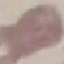
Summary:
  - Malaria status: uninfected
  - Image type: automatically extracted cell patch, resized to 64 × 64 pixels
  - Stain: Giemsa
  - Capture: smartphone through the microscope eyepiece
  - Preparation: thin blood smear